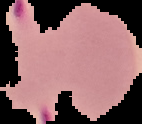 From a thin blood smear. Cell region segmented out of the field of view; the surrounding area is masked to black. Image is 142×124 pixels. Result: Plasmodium parasites detected.